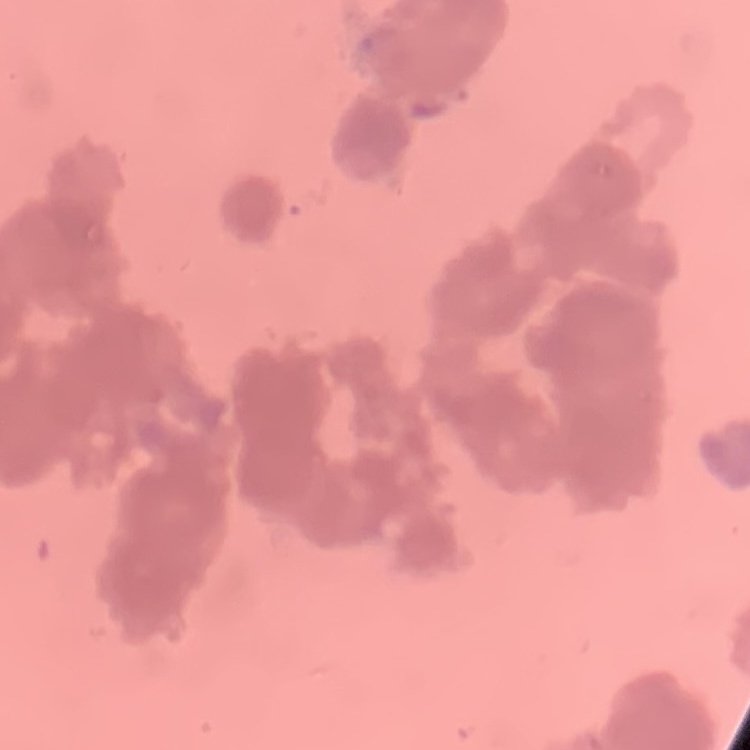

Summary:
  - Red blood cell morphology: rouleaux formation
  - Image type: square crop of a larger photomicrograph
  - Preparation: thin peripheral smear
  - Stain: Field's or Giemsa